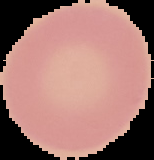
image size = 154×160 pixels
preparation = thin blood film
image type = segmented cell region with the area outside set to black
malaria status = uninfected